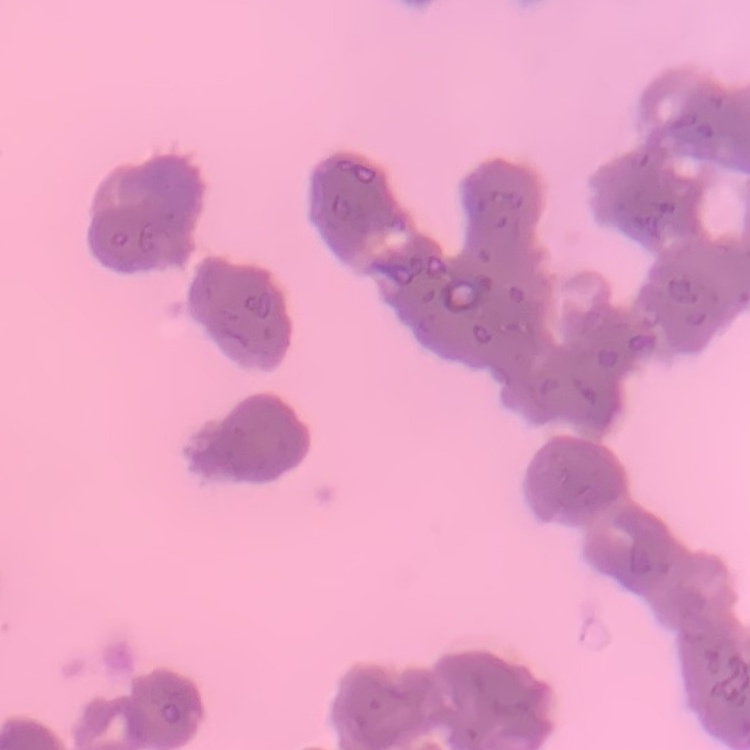

Summary:
  - Erythrocyte morphology: rouleaux formation
  - Image type: one tile cut from a larger photomicrograph
  - Preparation: thin peripheral smear
  - Stain: Field's or Giemsa